Classify this cell by malaria status.
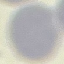
It is uninfected.

Summary:
  - Preparation: thin blood smear
  - Stain: Giemsa
  - Image type: automatically extracted cell patch, resized to 64 × 64 pixels
  - Capture: smartphone through the microscope eyepiece